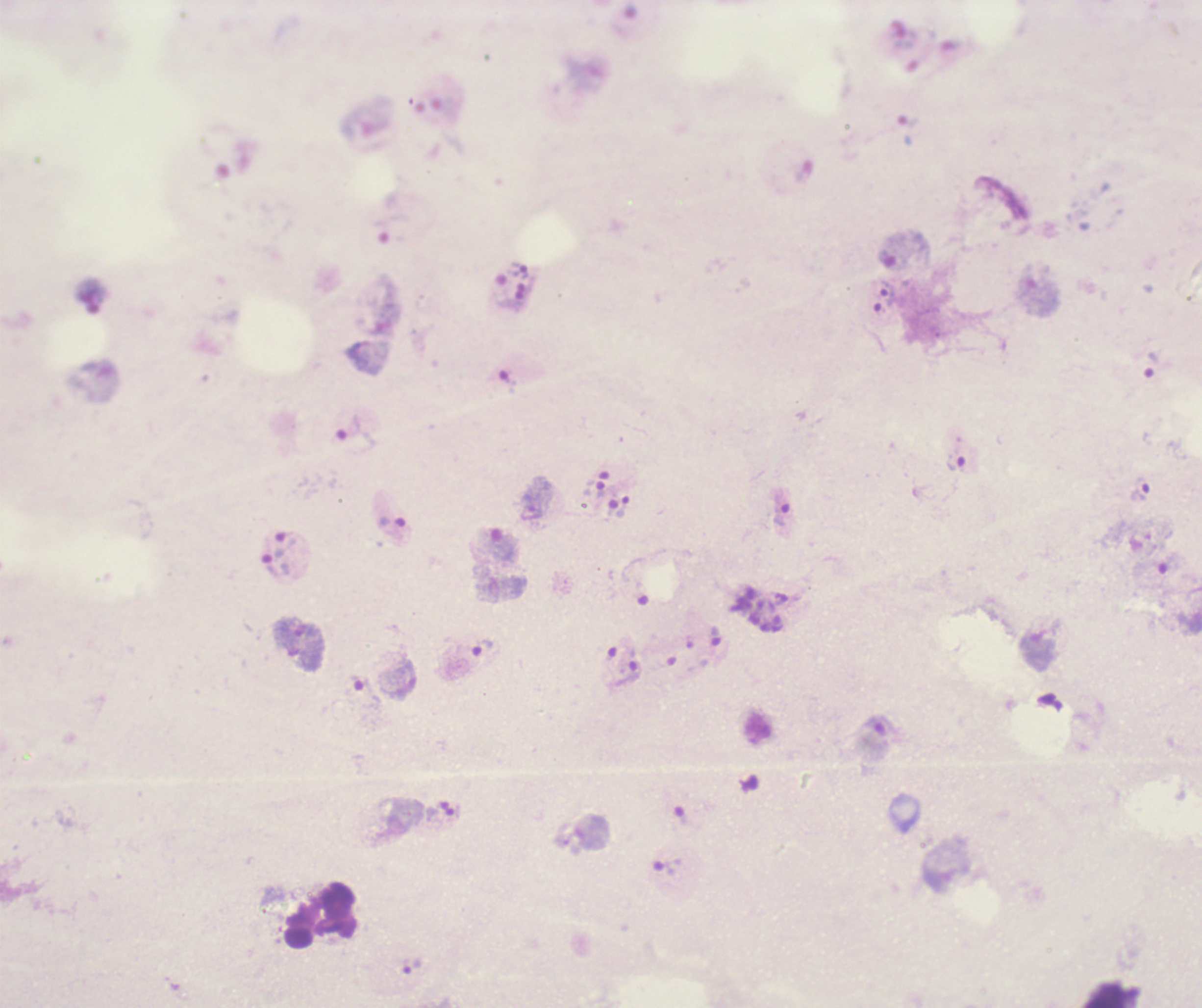

Approximate centers as [x, y] in pixels.
Summary:
  - Trophozoite locations: [887, 293], [1151, 364], [355, 429], [956, 463], [601, 489], [623, 506], [782, 510], [392, 522], [275, 565], [483, 648], [627, 676], [667, 867], [412, 965]
  - Leukocyte locations: [298, 938]
  - Gametocyte locations: [874, 738]
  - Life-cycle stages observed: trophozoite, gametocyte
  - Preparation: thick blood smear
  - Field of view: one from this slide
  - Background quality: unsatisfactory
  - Magnification: 100x
  - Image size: 1202×1008 pixels
  - Stain: Romanowsky
  - Context: previously used in an actual diagnosis
  - Coloration quality: bad
  - Result: malaria parasites identified